Give the position of every leukocyte visible.
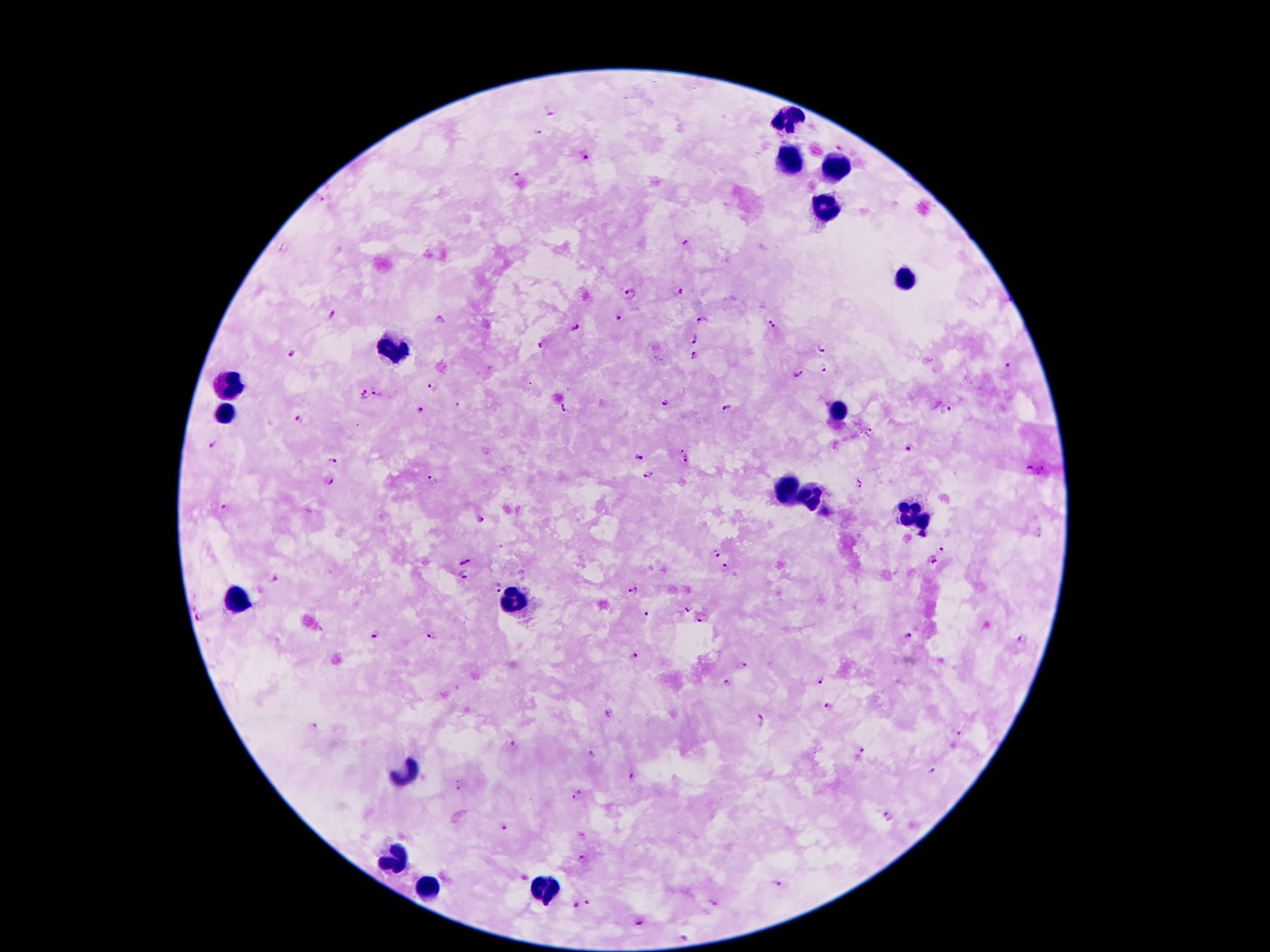
Approximate centers as {x, y} in pixels.
Leukocytes: {789, 120}, {787, 165}, {834, 167}, {824, 207}, {906, 280}, {393, 350}, {230, 387}, {835, 409}, {224, 414}, {786, 486}, {808, 498}, {915, 515}, {512, 599}, {239, 601}, {405, 774}, {396, 857}, {427, 889}, {543, 892}.

Summary:
  - Plasmodium parasite locations: {551, 112}, {538, 133}, {840, 145}, {585, 157}, {515, 177}, {320, 200}, {686, 243}, {285, 247}, {677, 291}, {630, 293}, {332, 315}, {616, 317}, {702, 321}, {439, 322}, {771, 324}, {575, 329}, {695, 338}, {541, 345}, {823, 347}, {294, 354}, {695, 355}, {1010, 364}, {823, 370}, {798, 373}, {431, 384}, {364, 393}, {378, 394}, {665, 401}, {457, 406}, {728, 408}, {564, 409}, {420, 411}, {944, 411}, {297, 419}, {869, 432}, {214, 443}, {683, 448}, {909, 448}, {637, 456}, {333, 460}, {687, 460}, {1036, 469}, {647, 475}, {328, 480}, {433, 480}, {860, 482}, {226, 507}, {481, 522}, {948, 546}, {712, 550}, {465, 560}, {929, 562}, {725, 568}, {465, 576}, {276, 578}, {497, 586}, {634, 590}, {685, 606}, {646, 614}, {199, 615}, {699, 618}, {375, 633}, {430, 636}, {909, 637}, {1022, 637}, {633, 656}, {744, 665}, {819, 678}, {727, 684}, {829, 706}, {609, 712}, {760, 719}, {314, 727}, {958, 733}, {513, 744}, {860, 750}, {592, 754}, {931, 770}, {633, 777}, {458, 785}, {581, 790}, {573, 798}, {891, 816}, {504, 827}, {582, 835}, {582, 858}, {778, 883}, {587, 903}, {715, 903}, {575, 905}, {640, 922}, {683, 939}
  - Image size: 1270×952 pixels
  - Patient malaria status: positive for Plasmodium falciparum
  - Preparation: thick blood film
  - Capture: smartphone through the microscope eyepiece
  - Stain: Giemsa
  - Magnification: 100x
  - Field of view: single